Assess this cell for malaria.
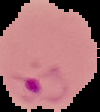

It is parasitized.

The area outside the segmented cell region is set to black. Image is 100×112 pixels. From a thin blood film.